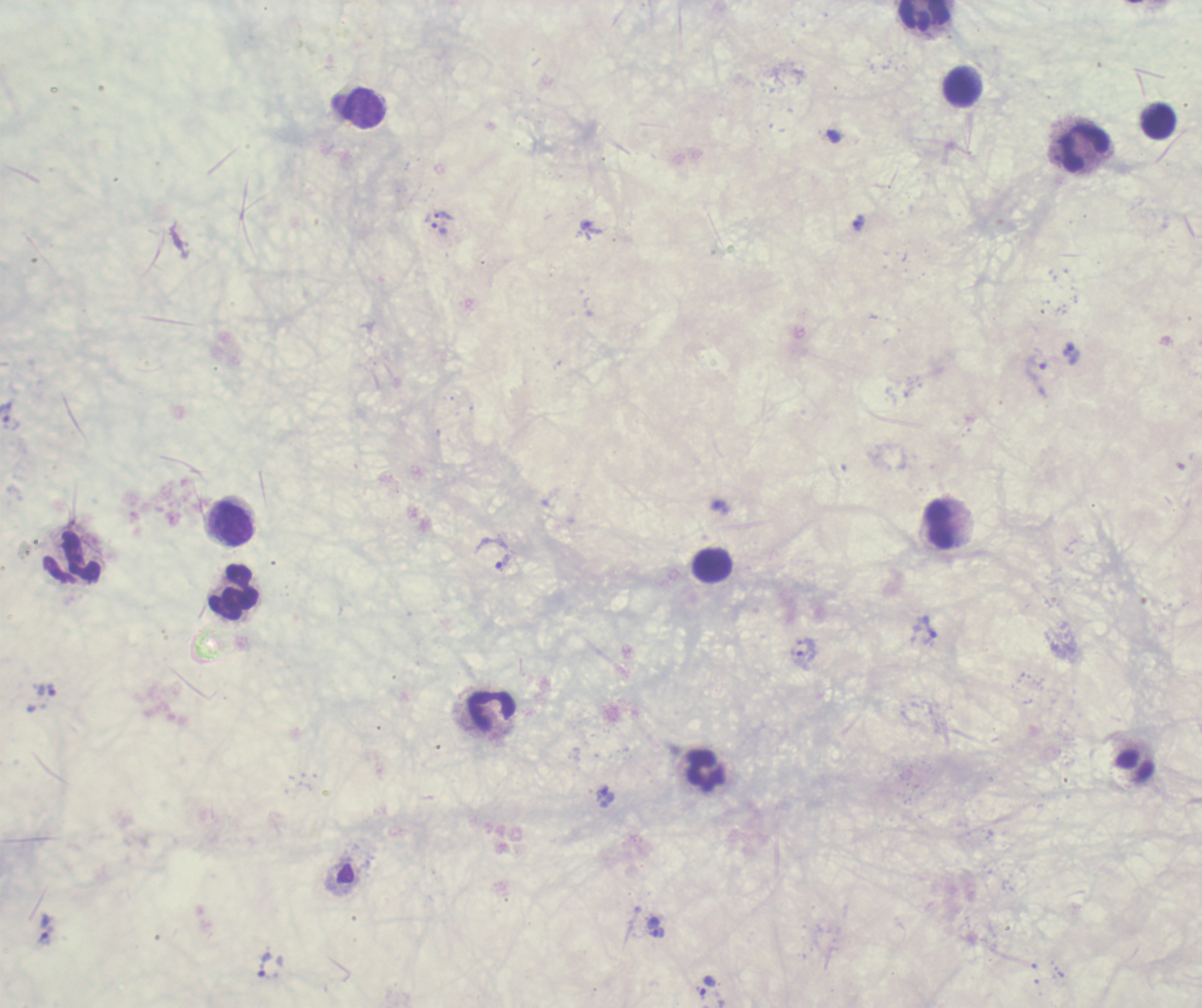

Approximate object centers, in pixels from the top-left corner.
Summary:
  - Trophozoite locations: (x=444, y=215), (x=858, y=223), (x=592, y=227), (x=439, y=230), (x=1071, y=353), (x=1036, y=370), (x=6, y=413), (x=493, y=554), (x=930, y=628), (x=803, y=657), (x=606, y=796), (x=656, y=932), (x=269, y=966), (x=709, y=986)
  - Leukocyte locations: (x=924, y=16), (x=961, y=87), (x=364, y=108), (x=1158, y=121), (x=1084, y=148), (x=232, y=524), (x=938, y=525), (x=72, y=557), (x=712, y=565), (x=233, y=592), (x=491, y=711), (x=705, y=772)
  - Context: previously used in a real diagnosis
  - Stain: Romanowsky
  - Result: malaria parasites identified
  - Preparation: thick blood smear
  - Field of view: one from this slide
  - Magnification: 100x
  - Coloration quality: bad
  - Image size: 1202×1008 pixels
  - Background quality: unsatisfactory